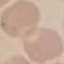

{
  "malaria_status": "uninfected",
  "preparation": "thin blood film",
  "capture": "smartphone through the microscope eyepiece",
  "image_type": "cell patch, automatically extracted from a larger field of view and resized to 64 × 64 pixels",
  "stain": "Giemsa"
}